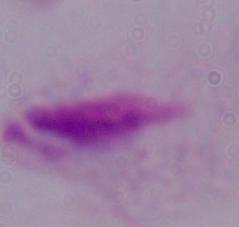
1000x magnification. Micrograph. A trichomonad is seen.